Give the position of every Plasmodium parasite.
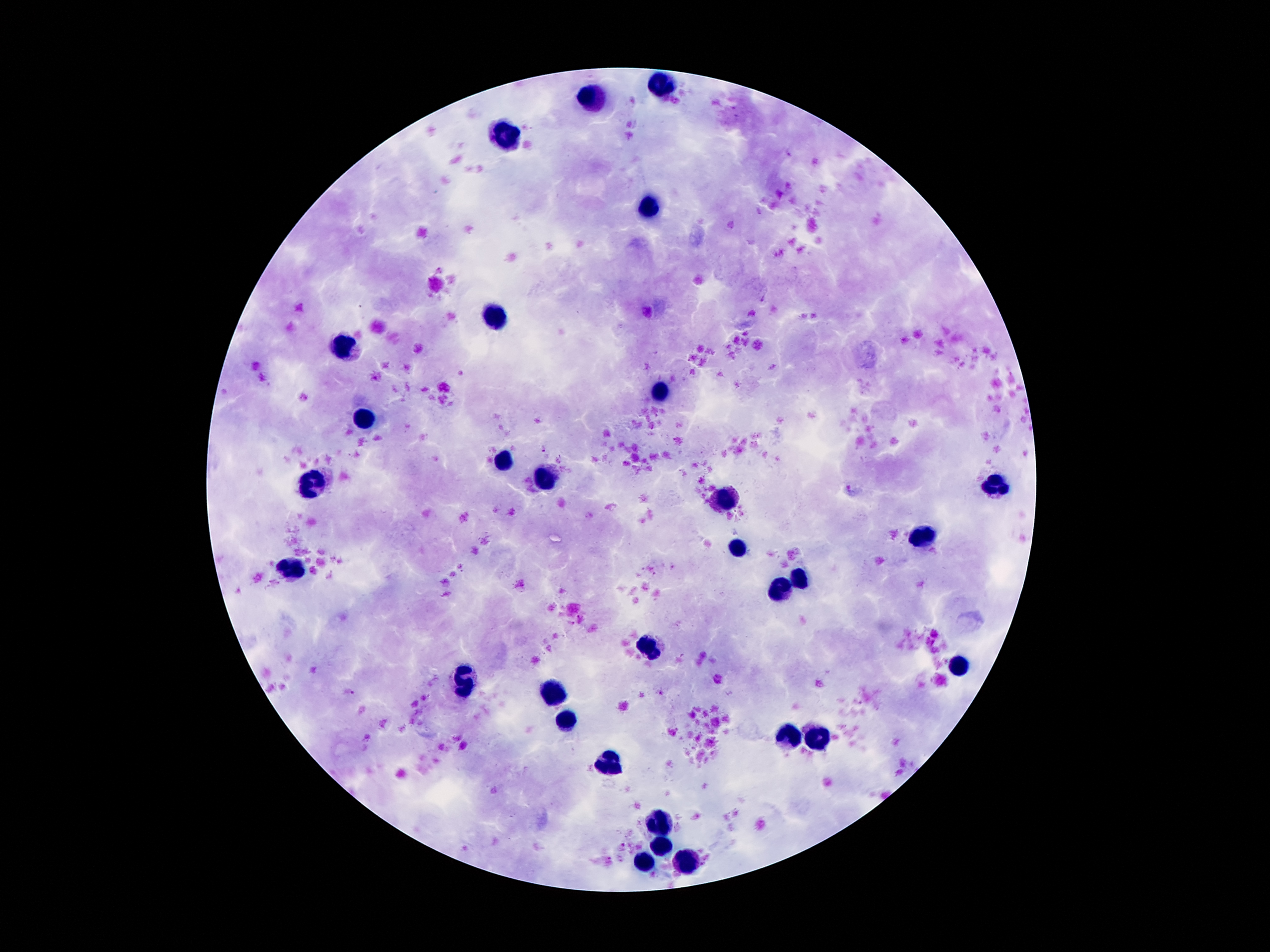

Approximate object centers, in pixels from the top-left corner.
Plasmodium parasites: (x=544, y=448), (x=349, y=692), (x=661, y=693).

Summary:
  - Leukocyte locations: (x=659, y=84), (x=595, y=98), (x=507, y=134), (x=647, y=207), (x=497, y=314), (x=344, y=348), (x=664, y=390), (x=364, y=420), (x=504, y=461), (x=544, y=479), (x=313, y=481), (x=997, y=487), (x=728, y=499), (x=922, y=538), (x=740, y=547), (x=292, y=565), (x=801, y=579), (x=781, y=586), (x=647, y=647), (x=959, y=665), (x=464, y=680), (x=553, y=695), (x=565, y=719), (x=791, y=739), (x=819, y=741), (x=608, y=763), (x=659, y=826), (x=660, y=846), (x=685, y=863), (x=644, y=864)
  - Field of view: one from this slide
  - Patient malaria status: positive for Plasmodium falciparum
  - Image size: 1270×952 pixels
  - Capture: smartphone through the microscope eyepiece
  - Stain: Giemsa
  - Preparation: thick peripheral-blood smear
  - Magnification: 100x